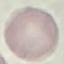

Malaria status: uninfected. Photographed with a smartphone camera at the microscope eyepiece. Cell patch, automatically extracted from a larger field of view and resized to 64 × 64 pixels. Thin smear of blood. Giemsa stain.